Name the parasite shown.
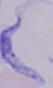

A trypanosome.

1000x magnification. Photomicrograph.